Outline each blood parasite and name the species.
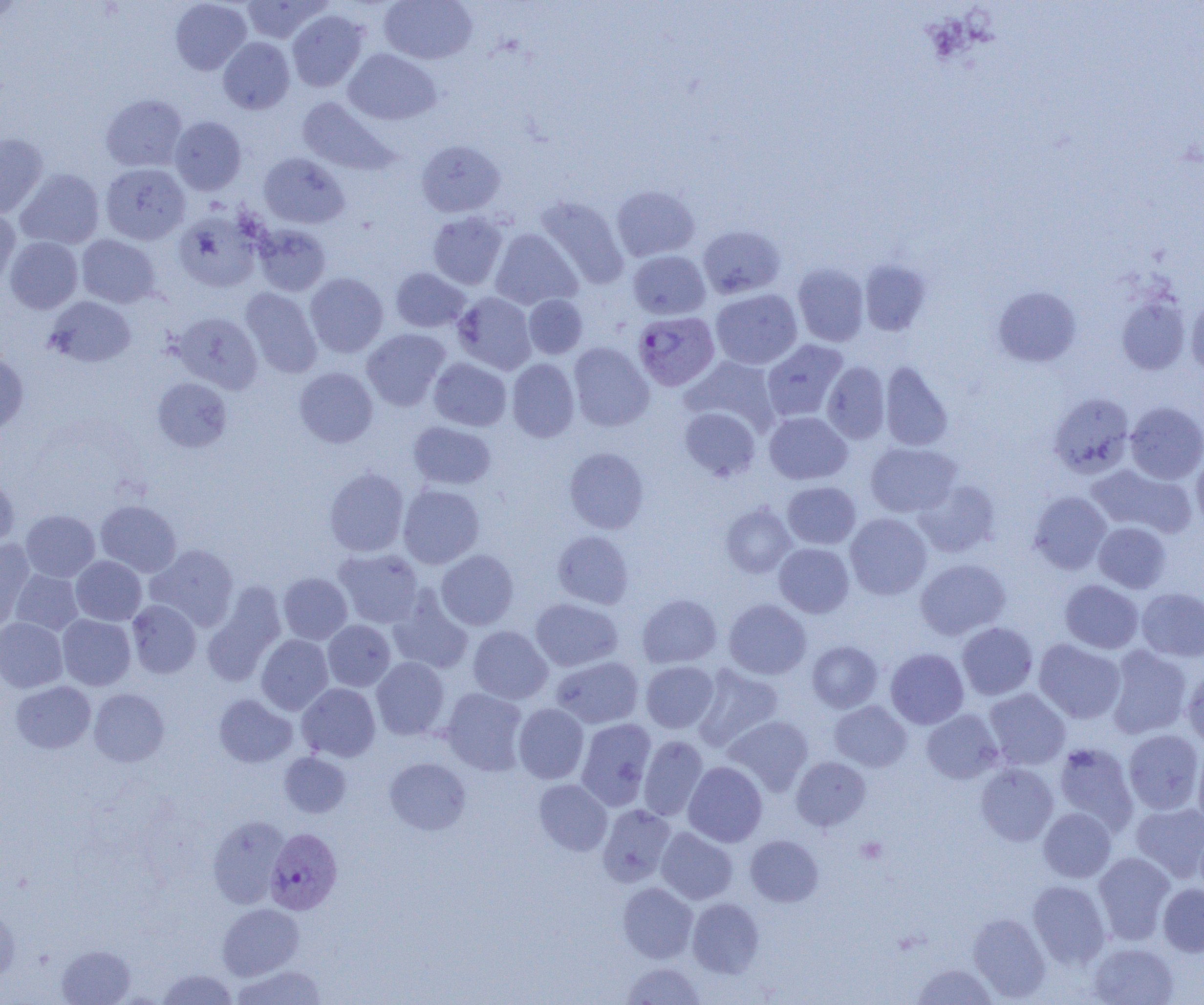

Approximate bounding boxes as [x1, y1, x2, y2] in pixels.
Plasmodium vivax-infected red blood cells: [633, 311, 719, 391], [264, 828, 343, 914].
No Plasmodium falciparum, Plasmodium ovale, Plasmodium malariae, Babesia divergens, or Trypanosoma brucei observed.

slide-level diagnosis = Plasmodium vivax
magnification = 1000x
uninfected red blood cell locations = approximate bounding boxes as [x1, y1, x2, y2] in pixels: [170, 0, 251, 75], [241, 0, 328, 43], [379, 0, 477, 65], [287, 10, 368, 91], [218, 37, 295, 114], [343, 49, 441, 126], [100, 94, 187, 171], [297, 96, 398, 176], [169, 116, 247, 195], [0, 133, 48, 218], [416, 139, 506, 217], [258, 152, 349, 228], [100, 163, 190, 244], [16, 169, 104, 249], [611, 185, 700, 261], [535, 195, 629, 289], [0, 207, 20, 291], [174, 210, 262, 292], [427, 211, 508, 290], [253, 224, 331, 296], [698, 225, 786, 299], [490, 228, 582, 310], [76, 235, 160, 308], [4, 237, 82, 313], [627, 250, 710, 320], [859, 259, 932, 335], [792, 263, 869, 346], [390, 267, 471, 332], [305, 273, 388, 357], [992, 286, 1082, 367], [241, 287, 322, 378], [710, 289, 802, 370], [453, 292, 536, 374], [524, 294, 588, 359], [45, 295, 136, 367], [1116, 295, 1190, 375], [1186, 296, 1204, 378], [172, 312, 263, 394], [362, 329, 450, 411], [762, 339, 848, 422], [568, 342, 654, 431], [0, 352, 28, 433], [682, 356, 780, 436], [429, 358, 511, 431], [507, 358, 579, 442], [822, 361, 890, 444], [880, 361, 953, 451], [294, 367, 378, 448], [152, 377, 232, 452], [1049, 392, 1134, 478], [1125, 401, 1204, 484], [679, 407, 761, 481], [764, 411, 852, 484], [408, 421, 496, 489], [866, 442, 961, 517], [564, 447, 649, 534], [1192, 452, 1204, 531], [1086, 463, 1194, 538], [324, 467, 409, 556], [0, 477, 19, 551], [914, 480, 1000, 558], [782, 481, 861, 549], [398, 484, 485, 569], [1029, 491, 1111, 574], [95, 500, 182, 577], [721, 503, 796, 578], [21, 510, 100, 582], [845, 513, 932, 600], [1093, 522, 1171, 593], [552, 530, 634, 609], [0, 541, 35, 632], [773, 543, 854, 618], [146, 544, 239, 631], [333, 548, 424, 628], [436, 550, 518, 630], [71, 556, 146, 625], [915, 558, 1010, 640], [10, 569, 83, 635], [278, 572, 352, 644], [1060, 580, 1144, 654], [203, 582, 286, 686], [387, 587, 473, 675], [1137, 588, 1204, 662], [637, 594, 721, 668], [530, 598, 622, 671], [724, 599, 811, 679], [127, 600, 201, 678], [57, 614, 135, 690], [0, 617, 67, 693], [323, 620, 395, 691], [957, 622, 1038, 700], [468, 626, 552, 704], [256, 634, 333, 715], [1034, 639, 1125, 724], [807, 641, 883, 713], [1106, 645, 1193, 739], [885, 648, 969, 729], [551, 656, 643, 728], [371, 657, 450, 740], [641, 661, 719, 733], [692, 664, 783, 752], [1182, 669, 1204, 749], [10, 681, 96, 753], [297, 683, 380, 762], [89, 688, 169, 767], [441, 688, 528, 775], [984, 688, 1070, 770], [214, 694, 298, 768], [829, 701, 911, 771], [513, 703, 589, 784], [921, 709, 1003, 784], [724, 715, 813, 795], [576, 718, 656, 810], [1123, 729, 1204, 815], [639, 735, 708, 820], [1053, 741, 1138, 832], [1193, 748, 1204, 831], [279, 752, 350, 818], [791, 756, 870, 831], [385, 757, 471, 835], [683, 761, 767, 847], [976, 763, 1058, 846], [534, 779, 612, 855], [1131, 802, 1204, 881], [597, 804, 676, 887], [1038, 807, 1116, 882], [207, 816, 290, 909], [656, 827, 738, 904], [745, 835, 823, 906], [1093, 852, 1175, 944], [1028, 880, 1110, 968], [618, 882, 698, 963], [1158, 883, 1204, 956], [687, 897, 764, 977], [0, 901, 20, 983], [217, 903, 304, 980], [967, 913, 1050, 1002], [1088, 942, 1179, 1005], [56, 944, 136, 1005], [622, 962, 706, 1004], [911, 962, 998, 1004], [231, 964, 327, 1004], [156, 969, 239, 1004]
preparation = thin blood smear
platelet locations = approximate bounding boxes as [x1, y1, x2, y2] in pixels: [856, 836, 887, 864]
modality = light microscopy
field of view = one of a larger specimen
image size = 1204×1005 pixels